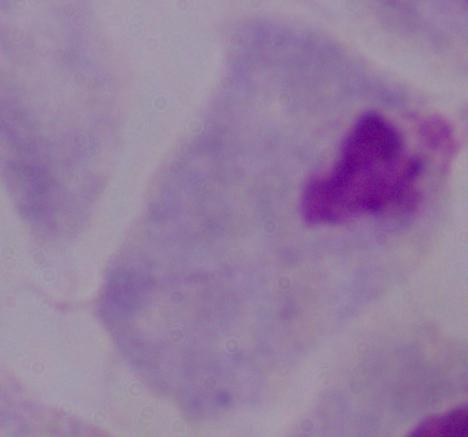

{
  "modality": "micrograph",
  "magnification": "1000x",
  "identification": "trichomonad"
}